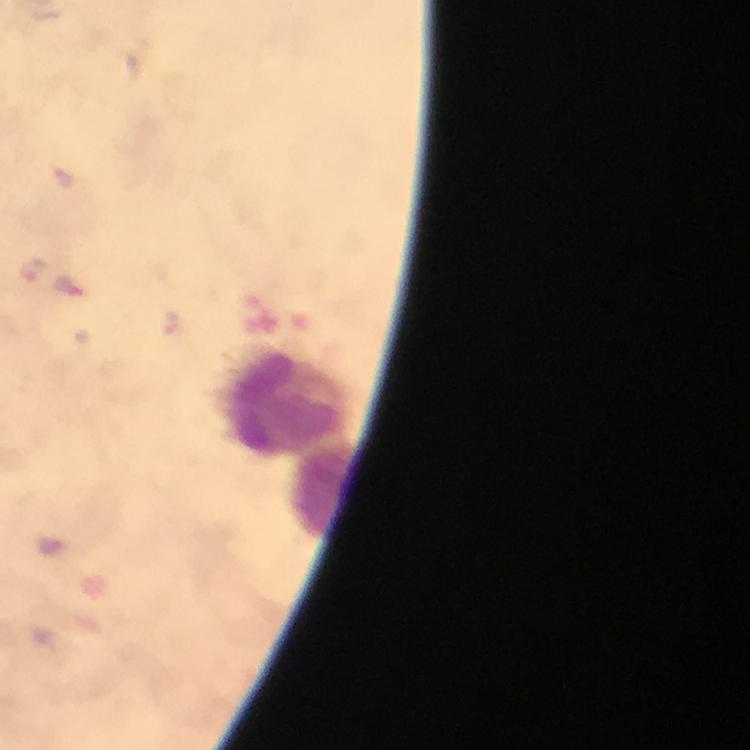

{
  "magnification": "100x",
  "capture": "smartphone mounted on the microscope",
  "immersion_oil": "used",
  "preparation": "thick blood film",
  "stain": "Giemsa",
  "context": "from a diagnostic examination for malaria",
  "plasmodium_parasite_locations": "approximate centers as (x, y) in pixels: (32, 269), (69, 287), (51, 546)",
  "cropped_from": "one field of view",
  "leukocyte_locations": "approximate centers as (x, y) in pixels: (286, 405), (321, 491)",
  "image_size": "750×750 pixels"
}